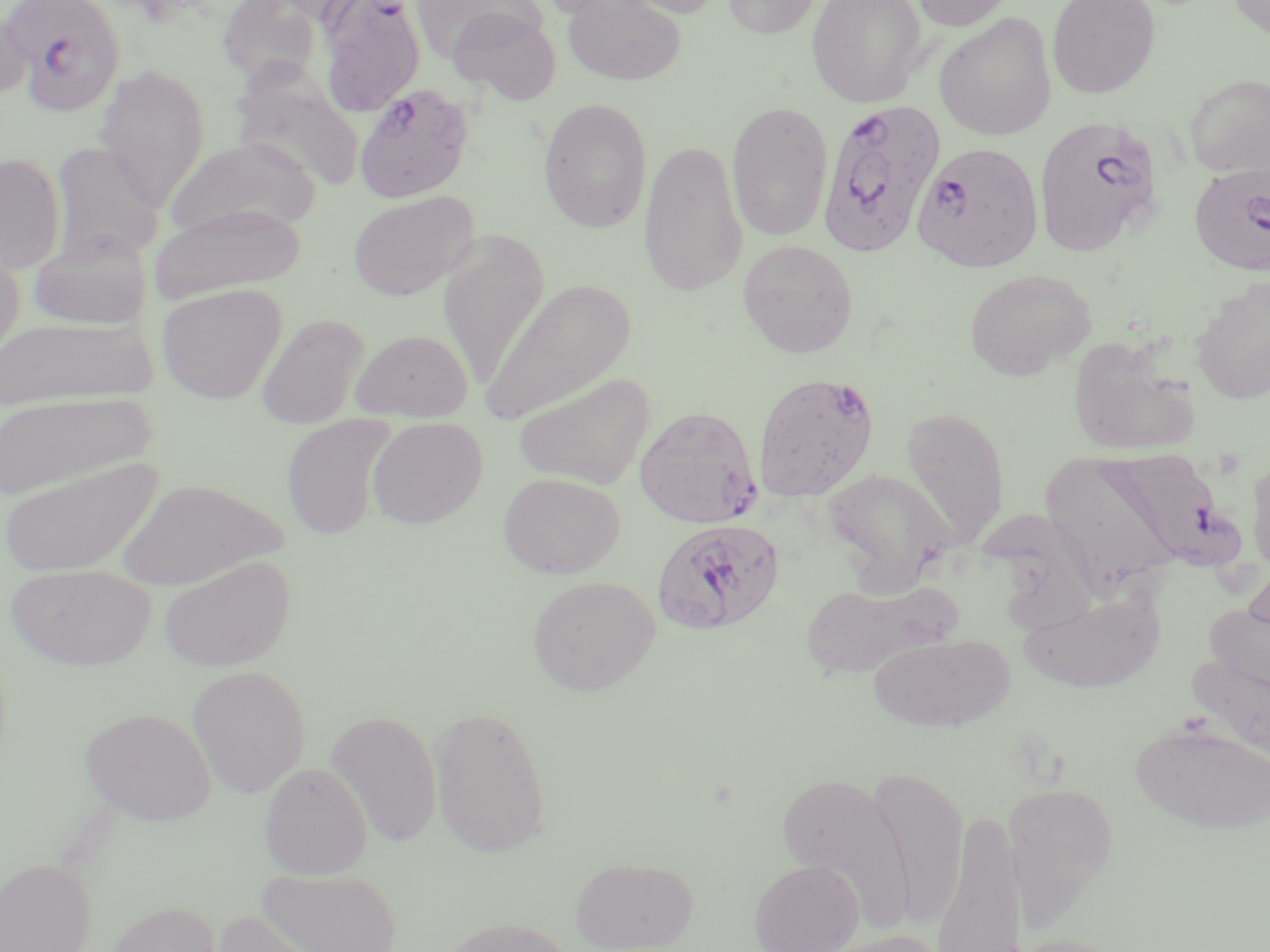

slide-level diagnosis = Plasmodium falciparum
image size = 1270×952 pixels
uninfected red blood cell locations = approximate bounding boxes as (x1, y1, x2, y2) in pixels: (217, 0, 320, 87), (261, 0, 370, 26), (563, 0, 685, 85), (613, 0, 729, 19), (721, 0, 823, 39), (807, 0, 926, 106), (907, 0, 1016, 31), (1047, 0, 1161, 99), (1227, 0, 1270, 41), (317, 1, 425, 116), (412, 1, 544, 62), (447, 7, 562, 105), (0, 10, 32, 103), (934, 12, 1057, 141), (94, 64, 210, 212), (231, 69, 366, 192), (1184, 74, 1270, 179), (537, 97, 653, 233), (726, 99, 833, 241), (164, 136, 320, 243), (638, 139, 747, 298), (49, 141, 165, 266), (0, 152, 66, 273), (348, 191, 478, 301), (151, 202, 308, 301), (438, 228, 550, 391), (30, 231, 148, 330), (0, 236, 25, 365), (737, 239, 858, 358), (963, 267, 1097, 381), (1189, 276, 1270, 405), (480, 278, 638, 425), (157, 283, 287, 404), (255, 313, 370, 429), (0, 316, 155, 411), (350, 328, 473, 422), (1067, 337, 1200, 459), (513, 371, 656, 490), (0, 391, 155, 503), (900, 406, 1010, 549), (281, 415, 396, 541), (366, 417, 488, 529), (1246, 451, 1270, 575), (1040, 452, 1182, 589), (0, 455, 165, 578), (823, 468, 955, 592), (497, 472, 625, 579), (114, 478, 287, 589), (158, 555, 295, 673), (4, 564, 156, 671), (526, 574, 661, 696), (800, 580, 954, 679), (1016, 590, 1166, 694), (1204, 595, 1269, 707), (867, 631, 1015, 733), (1185, 641, 1270, 767), (187, 664, 311, 798), (427, 705, 552, 859), (80, 706, 217, 826), (325, 708, 442, 848), (1130, 718, 1270, 834), (258, 761, 373, 880), (868, 766, 969, 928), (775, 769, 915, 933), (1002, 781, 1119, 929), (932, 807, 1025, 950), (570, 856, 699, 952), (0, 857, 96, 952), (748, 858, 864, 952), (256, 868, 403, 952), (100, 900, 222, 952), (203, 909, 330, 952), (443, 916, 576, 952), (816, 928, 950, 952)
field of view = one of a larger specimen
preparation = thin blood smear
modality = optical microscopy
magnification = 1000x
Plasmodium falciparum-infected red blood cell locations = approximate bounding boxes as (x1, y1, x2, y2) in pixels: (1, 0, 126, 116), (353, 83, 474, 203), (816, 97, 947, 258), (1033, 115, 1167, 258), (911, 141, 1044, 272), (1188, 161, 1270, 277), (752, 371, 881, 503), (634, 405, 762, 528), (1101, 448, 1237, 572), (651, 517, 785, 636)
stain = May-Grünwald-Giemsa